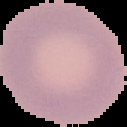
Summary:
  - Malaria status: uninfected
  - Image type: cell region segmented out of the field of view; surrounding area masked to black
  - Preparation: thin blood film
  - Image size: 127×127 pixels